State which parasite is depicted.
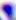

This is Toxoplasma gondii.

{
  "magnification": "400x",
  "modality": "micrograph"
}